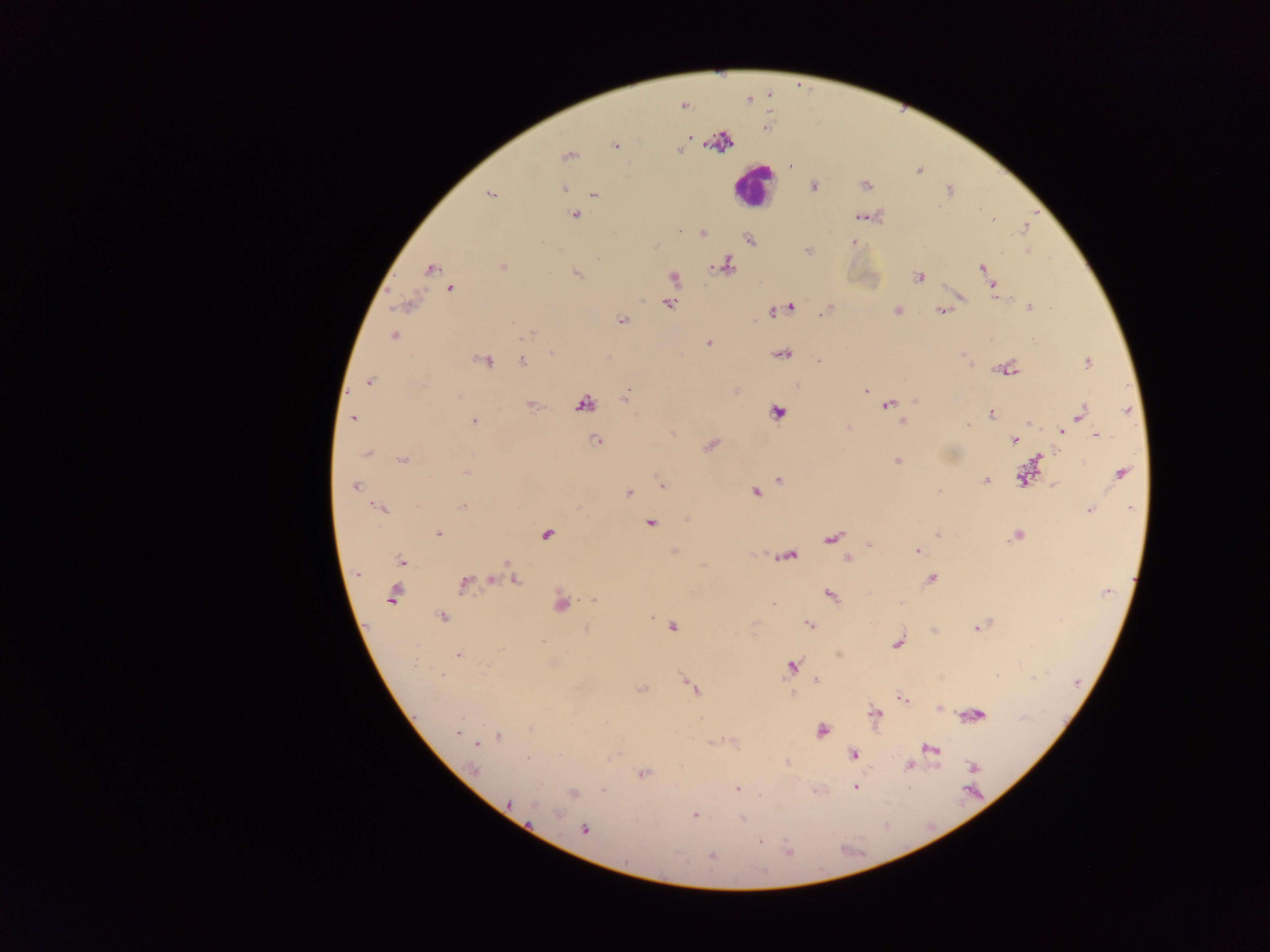

Approximate centers as {x, y} in pixels. Malaria parasite locations: {688, 141}, {681, 152}, {566, 155}, {564, 188}, {814, 189}, {490, 195}, {592, 195}, {575, 215}, {678, 230}, {703, 232}, {852, 242}, {655, 245}, {806, 249}, {727, 264}, {503, 265}, {712, 266}, {979, 266}, {431, 268}, {577, 273}, {920, 277}, {994, 284}, {450, 289}, {995, 296}, {964, 297}, {642, 298}, {670, 303}, {1029, 305}, {394, 307}, {793, 307}, {897, 309}, {771, 311}, {939, 311}, {622, 319}, {527, 334}, {394, 337}, {708, 342}, {551, 351}, {484, 361}, {521, 361}, {819, 361}, {1087, 361}, {369, 382}, {629, 390}, {866, 390}, {626, 395}, {459, 396}, {529, 405}, {887, 406}, {991, 413}, {1079, 414}, {353, 418}, {473, 422}, {903, 422}, {1029, 423}, {848, 426}, {968, 426}, {672, 432}, {1060, 432}, {1096, 434}, {1012, 439}, {595, 440}, {709, 446}, {368, 454}, {402, 458}, {897, 460}, {466, 471}, {655, 472}, {1120, 473}, {657, 476}, {779, 480}, {986, 480}, {355, 486}, {661, 486}, {1055, 487}, {756, 491}, {629, 492}, {463, 506}, {377, 507}, {1090, 511}, {686, 518}, {653, 521}, {437, 534}, {547, 534}, {870, 542}, {915, 550}, {675, 551}, {775, 557}, {848, 558}, {403, 561}, {356, 574}, {933, 578}, {513, 579}, {465, 585}, {392, 595}, {831, 595}, {592, 599}, {901, 604}, {560, 605}, {773, 606}, {441, 616}, {809, 625}, {673, 627}, {586, 629}, {976, 629}, {545, 641}, {898, 643}, {499, 648}, {458, 654}, {417, 663}, {790, 665}, {440, 677}, {816, 679}, {691, 686}, {792, 693}, {903, 699}, {529, 727}, {821, 730}, {455, 733}, {499, 737}, {479, 741}, {711, 741}, {851, 754}, {528, 758}, {909, 766}, {476, 768}, {643, 773}, {854, 788}, {737, 789}, {602, 791}, {510, 803}, {694, 815}, {741, 820}, {585, 830}, {758, 843}, {710, 856}. Leukocyte locations: {748, 189}. Thick blood film. Single field of view. Image is 1270×952 pixels. Collected in Ghana. Mobile-phone photograph taken through the microscope.